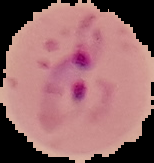

Summary:
  - Preparation: thin blood smear
  - Malaria status: parasitized
  - Image size: 154×163 pixels
  - Image type: cell region segmented out of the field of view; surrounding area masked to black